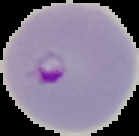
Summary:
  - Image type: segmented cell region with the area outside set to black
  - Preparation: thin blood smear
  - Image size: 139×136 pixels
  - Result: Plasmodium parasites detected